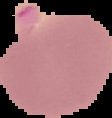

Summary:
  - Preparation: thin blood smear
  - Image type: segmented cell region with the area outside set to black
  - Result: malaria parasites identified
  - Image size: 112×118 pixels